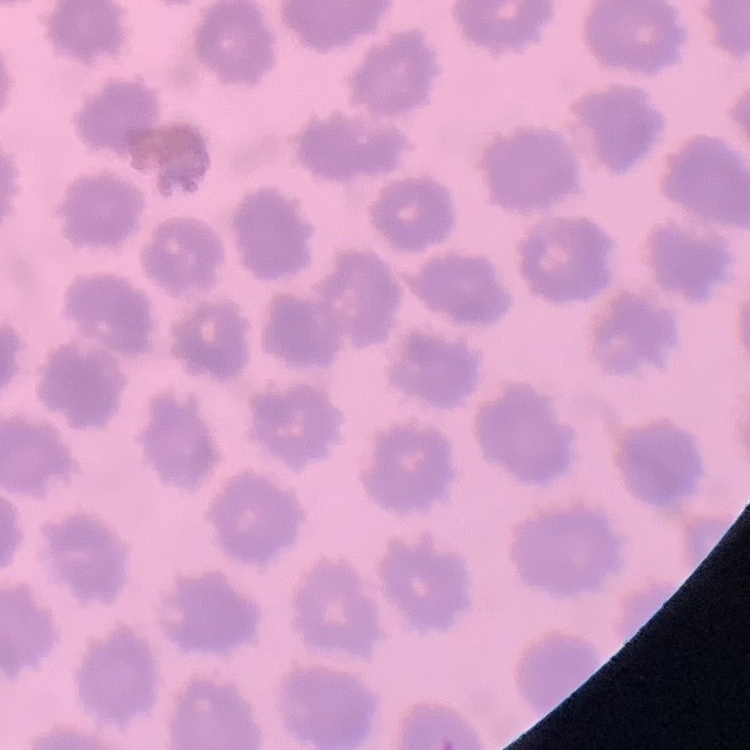
The red blood cells show no rouleaux formation. Thin blood film. Field's or Giemsa stain. One tile cut from a larger photomicrograph.